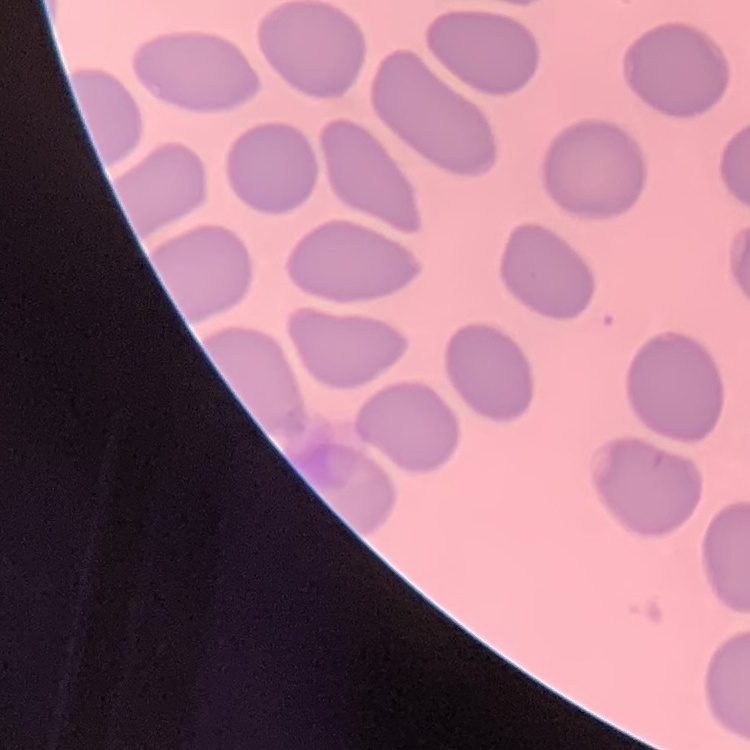

Summary:
  - Red blood cell morphology: no rouleaux formation
  - Preparation: thin blood smear
  - Image type: square crop of a larger photomicrograph
  - Stain: Field's or Giemsa